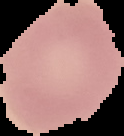
Summary:
  - Image size: 124×136 pixels
  - Preparation: thin blood film
  - Image type: segmented cell region with the area outside set to black
  - Result: no malaria parasites detected